Identify the preparation type.
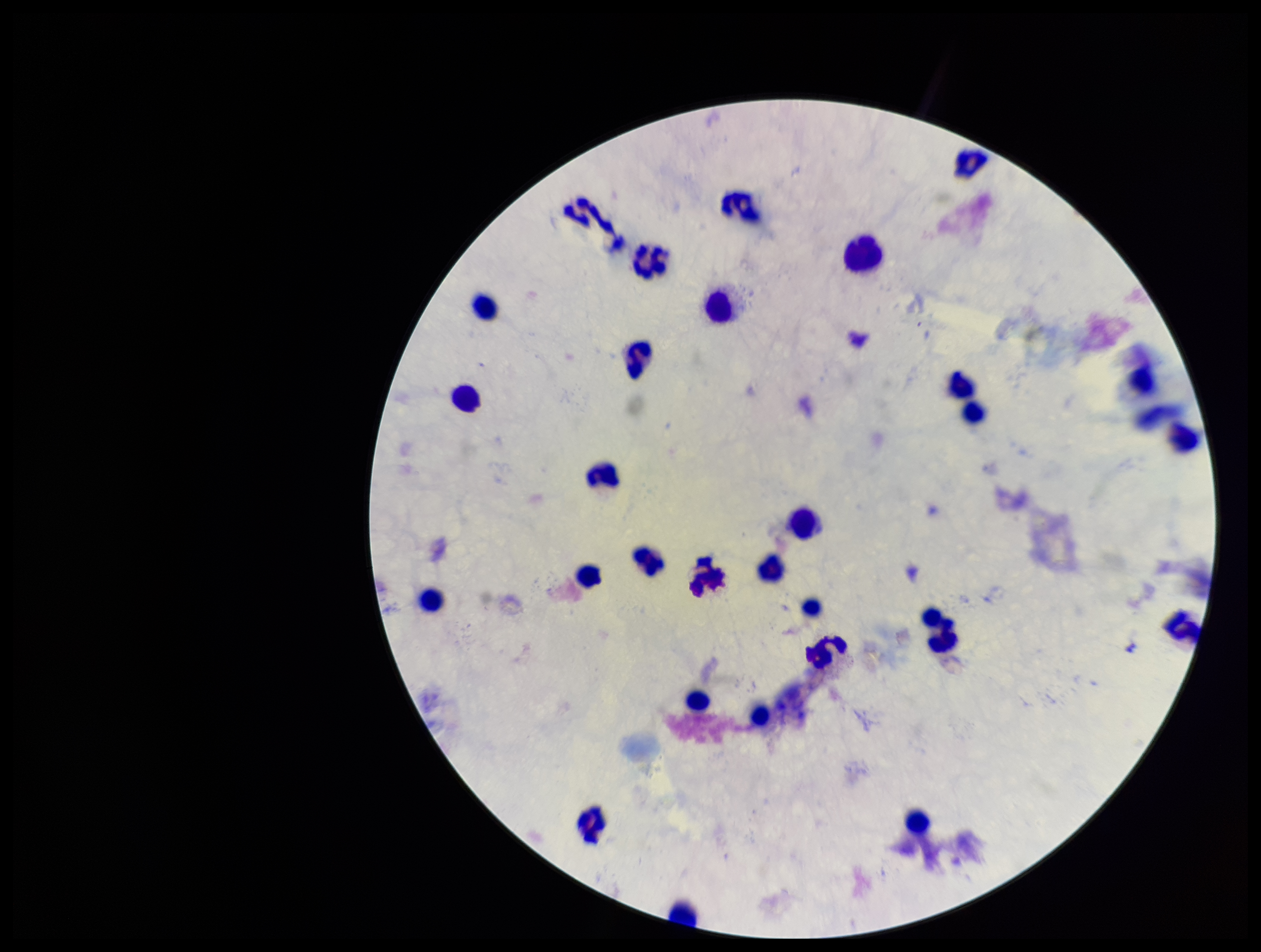
A thick smear.

Parasite count: 0. Giemsa stain. Leukocyte count: 29. Smartphone photograph taken through the eyepiece of a microscope. Patient malaria status: negative. Plasmodium parasites: none identified. One field from this slide. Image is 1261×952 pixels.